Name the blood parasite species.
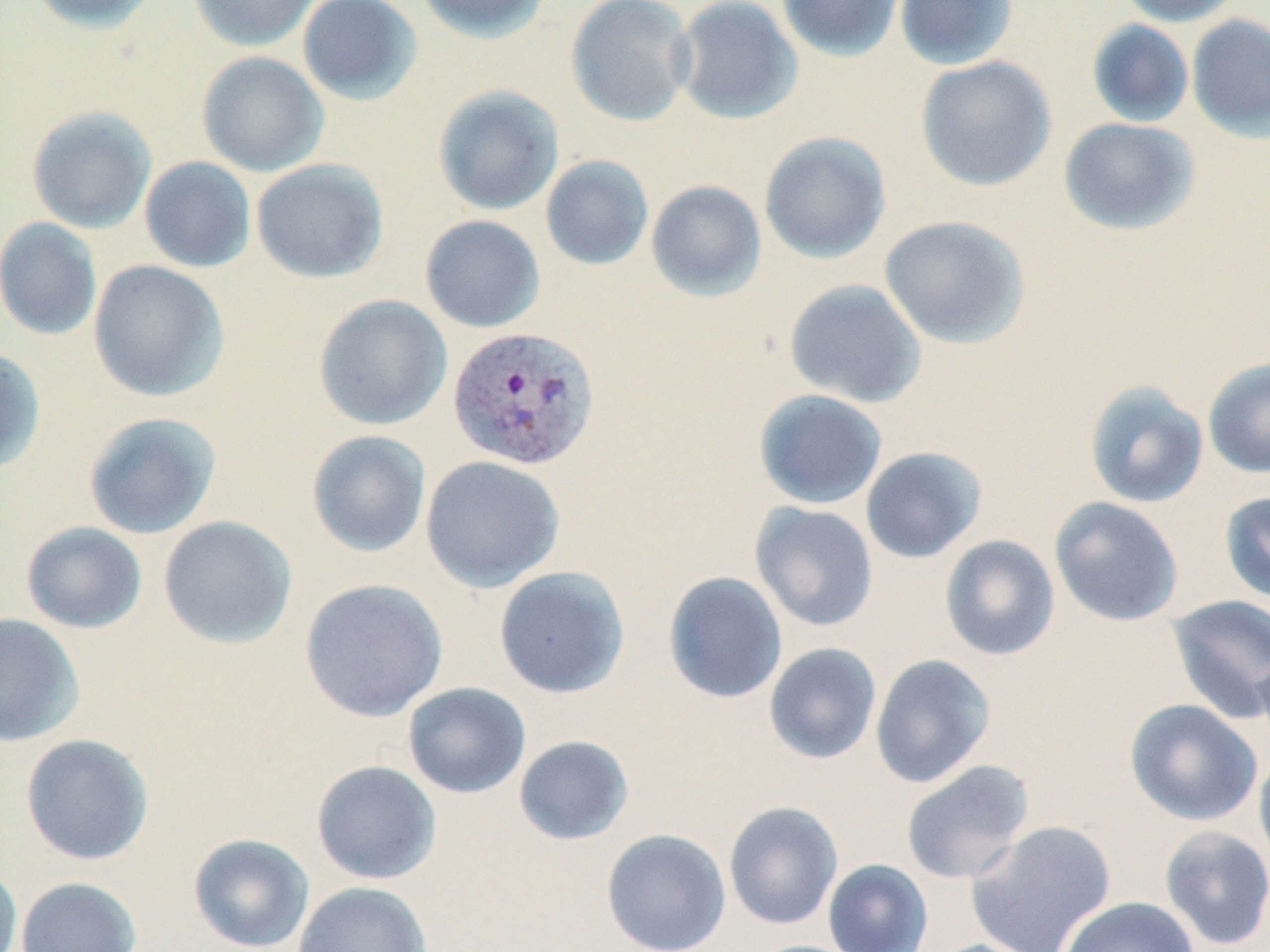

Plasmodium vivax.

{
  "preparation": "thin blood smear",
  "uninfected_red_blood_cell_locations": "approximate bounding boxes as [x1, y1, x2, y2] in pixels: [29, 0, 160, 34], [188, 0, 321, 51], [297, 0, 423, 106], [414, 0, 551, 43], [566, 0, 696, 126], [671, 0, 803, 124], [776, 0, 905, 62], [894, 0, 1019, 71], [1115, 0, 1246, 26], [1186, 14, 1270, 141], [1086, 19, 1194, 128], [196, 51, 329, 177], [916, 55, 1057, 192], [432, 84, 564, 216], [26, 105, 157, 234], [1058, 117, 1200, 236], [759, 131, 891, 264], [540, 155, 654, 270], [139, 156, 256, 273], [251, 158, 388, 283], [645, 180, 766, 302], [420, 214, 545, 333], [879, 215, 1031, 349], [0, 217, 103, 341], [87, 260, 229, 402], [784, 278, 927, 408], [313, 294, 452, 430], [0, 345, 46, 474], [1203, 357, 1270, 478], [1084, 381, 1209, 509], [753, 389, 887, 509], [82, 411, 222, 539], [306, 429, 431, 558], [860, 447, 987, 564], [420, 455, 565, 592], [1219, 490, 1270, 605], [1049, 497, 1184, 626], [749, 502, 878, 632], [158, 515, 297, 649], [20, 521, 147, 634], [939, 535, 1060, 661], [493, 566, 630, 699], [662, 570, 788, 704], [299, 578, 448, 722], [1166, 593, 1270, 724], [0, 613, 84, 747], [763, 642, 882, 765], [1253, 650, 1270, 758], [870, 654, 995, 788], [402, 682, 532, 799], [1124, 699, 1262, 827], [20, 734, 154, 865], [512, 735, 634, 846], [1253, 749, 1270, 875], [901, 759, 1034, 885], [311, 760, 442, 885], [723, 801, 843, 930], [965, 820, 1116, 952], [1159, 826, 1270, 950], [601, 828, 731, 952], [188, 833, 315, 952], [823, 859, 933, 952], [0, 860, 23, 952], [15, 876, 141, 952], [292, 881, 432, 952], [1060, 896, 1199, 952], [917, 938, 1046, 952], [746, 939, 864, 952]",
  "field_of_view": "single",
  "image_size": "1270×952 pixels",
  "modality": "light microscopy",
  "magnification": "1000x",
  "plasmodium_vivax_infected_red_blood_cell_locations": "approximate bounding boxes as [x1, y1, x2, y2] in pixels: [447, 325, 601, 471]",
  "stain": "May-Grünwald-Giemsa"
}